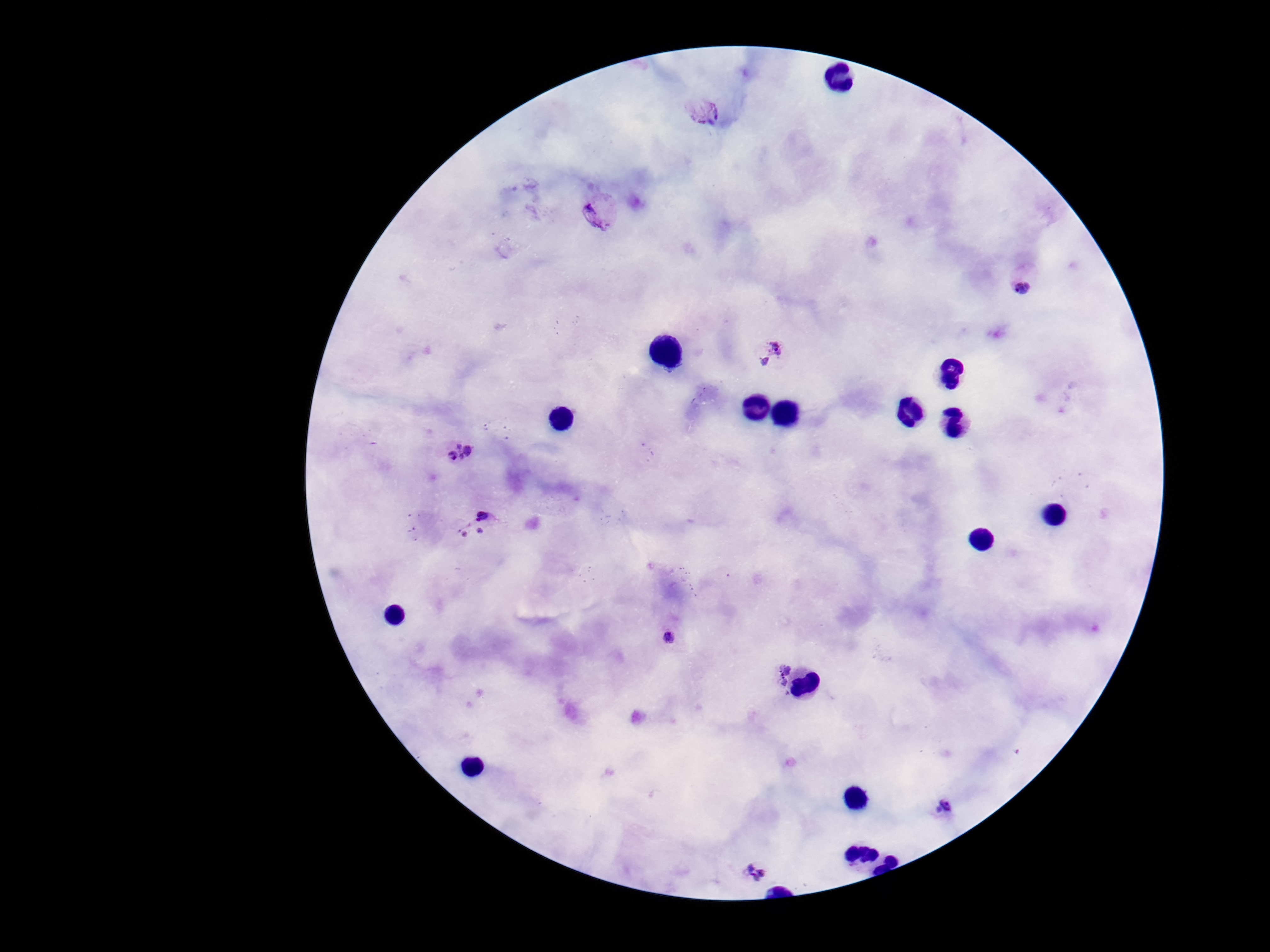

Approximate centers as {x, y} in pixels. Plasmodium parasite locations: {702, 110}, {602, 210}, {1025, 279}, {767, 350}, {460, 452}, {481, 513}, {480, 530}, {463, 535}, {669, 638}, {778, 673}, {941, 810}, {757, 870}. Image is 1270×952 pixels. Patient malaria status: positive. 100x magnification. Giemsa-stained preparation. Thick blood smear. One field from this slide. Smartphone photograph taken through the microscope eyepiece.